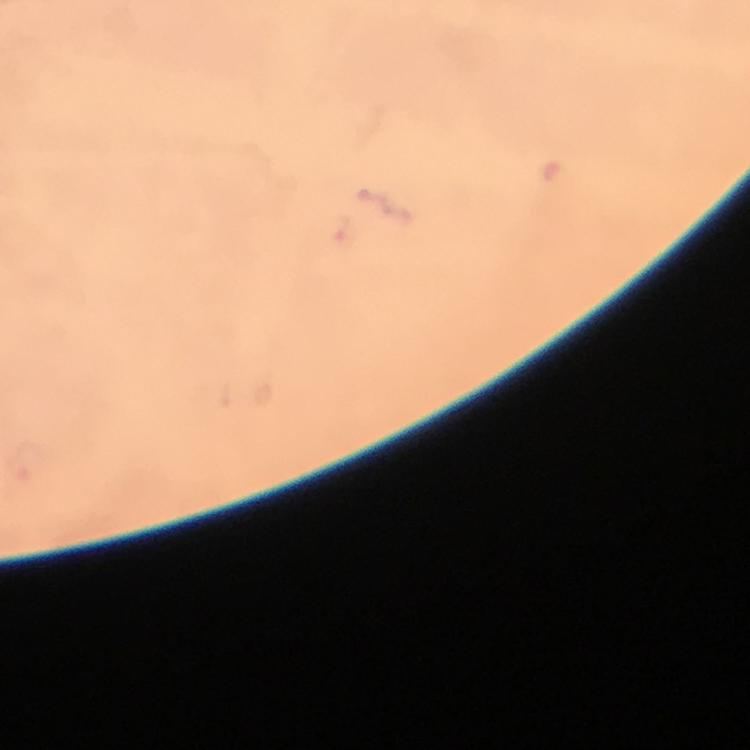

cropped_from: a single field of view
magnification: 100x
context: from a malaria diagnostic workup
stain: Giemsa
preparation: thick blood smear
image_size: 750×750 pixels
capture: smartphone camera through the microscope
plasmodium_parasite_locations: 'approximate centers as {x, y} in pixels: {345, 232}'
immersion_oil: applied